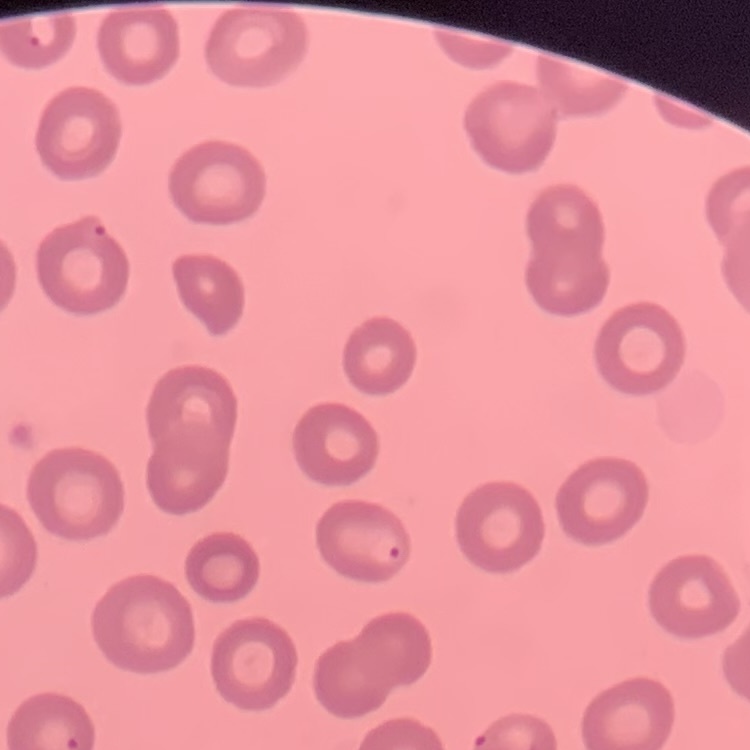
red blood cell morphology = no rouleaux formation
preparation = thin peripheral smear
image type = square crop of a larger photomicrograph
stain = Field's or Giemsa